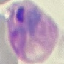
result = malaria parasites identified
preparation = thin blood smear
stain = Giemsa
image type = automatically extracted cell patch, resized to 64 × 64 pixels
capture = smartphone through the microscope eyepiece